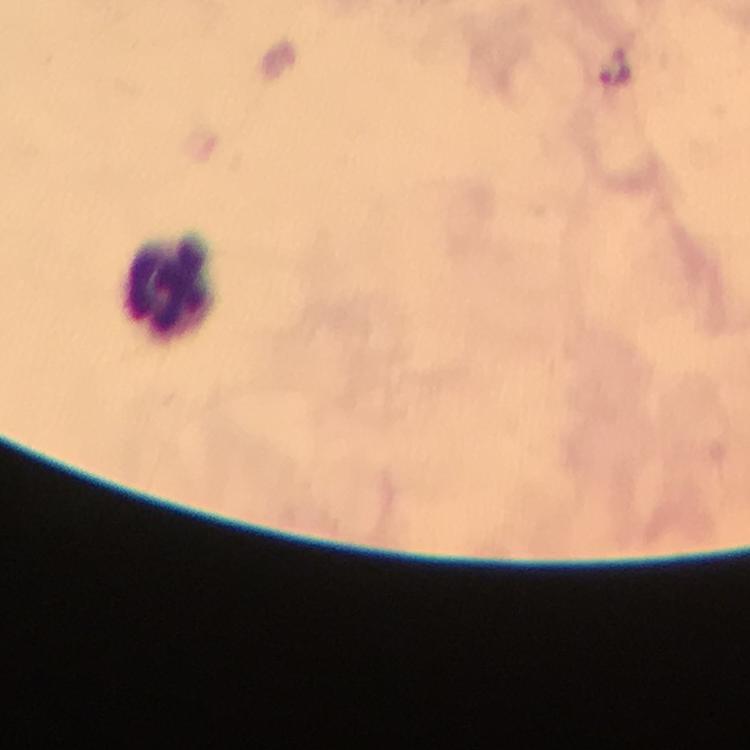

cropped from = one field of view
magnification = 100x
capture = smartphone mounted on the microscope
image size = 750×750 pixels
immersion oil = used
leukocyte locations = approximate centers as (x, y) in pixels: (168, 285)
preparation = thick smear
context = from a malaria diagnostic workup
Plasmodium parasite locations = approximate centers as (x, y) in pixels: (618, 76)
stain = Giemsa